Assess for malaria.
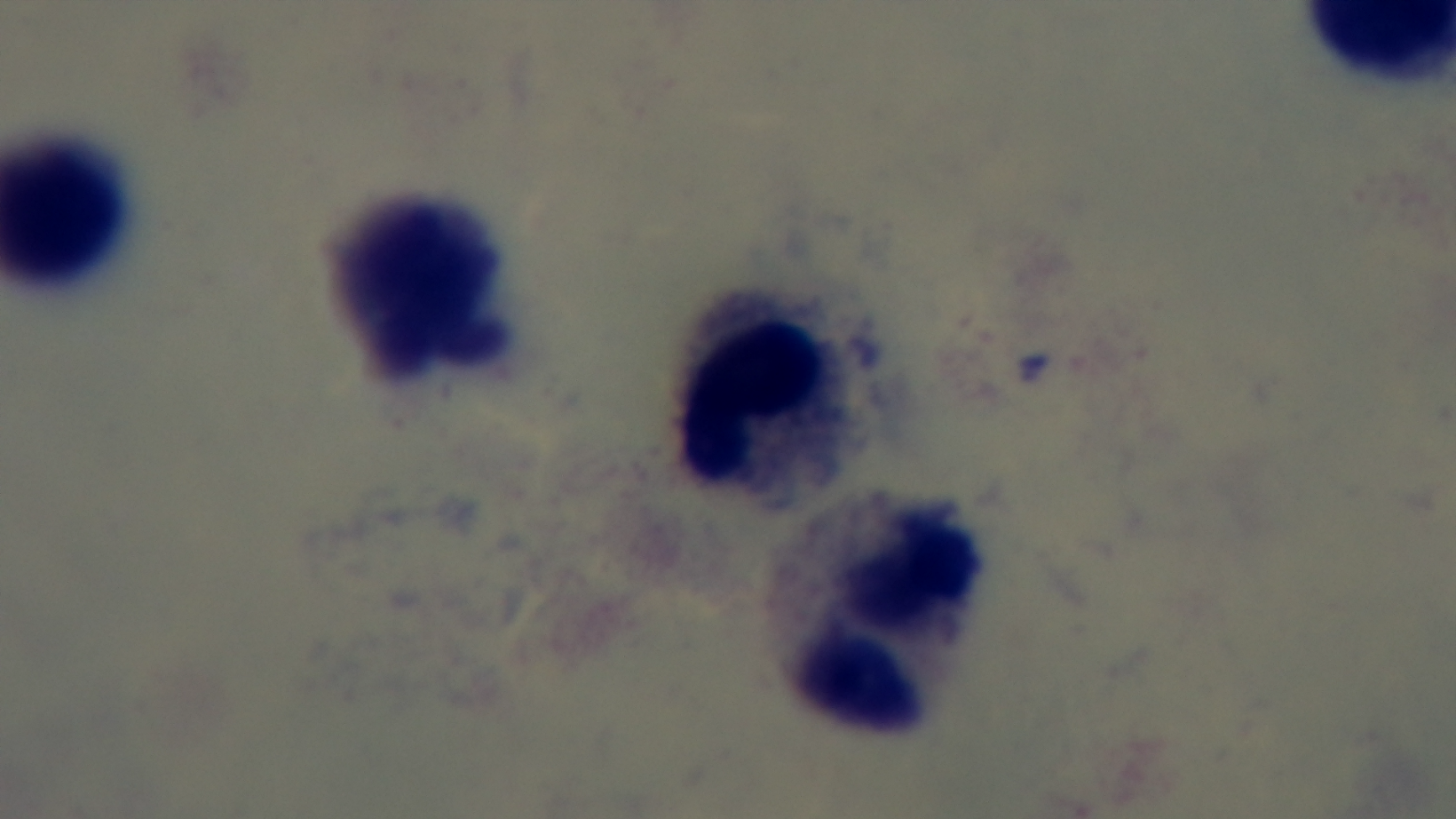
It is uninfected.

Summary:
  - Objective: 100x oil immersion
  - Field of view: one from the slide
  - Modality: light microscopy
  - Capture: mounted 4K digital camera
  - Stain: Giemsa
  - Preparation: thick smear